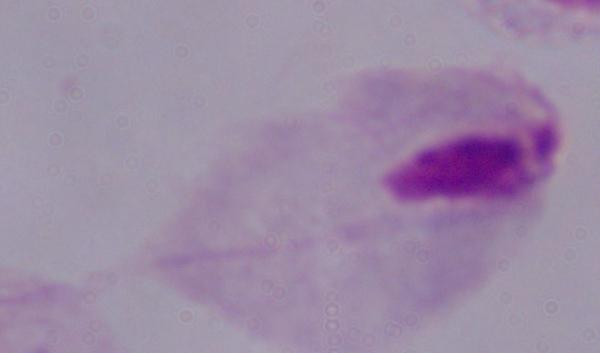
Micrograph. Captured at 1000x magnification. A trichomonad is seen.